Describe the morphology of the erythrocytes.
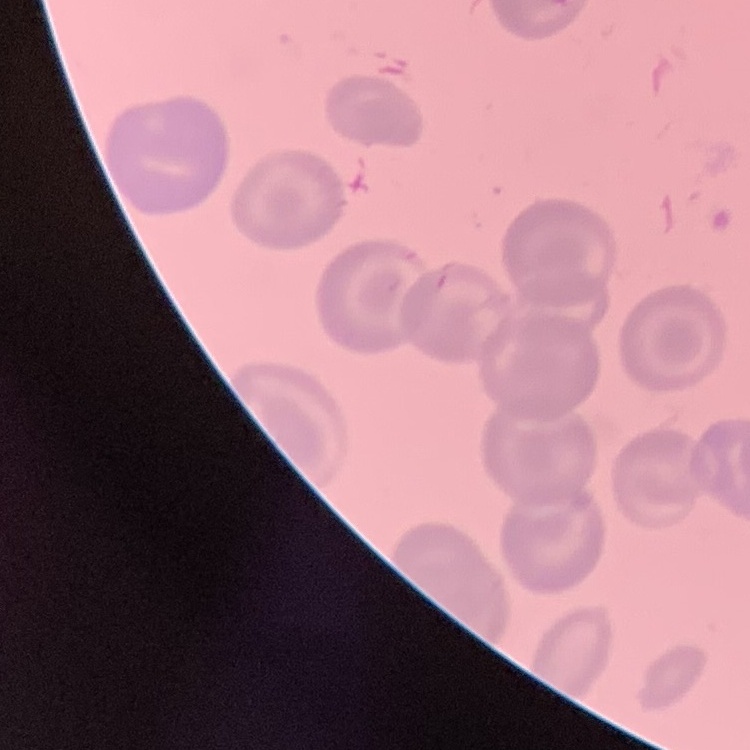
They show no rouleaux formation.

Summary:
  - Stain: Field's or Giemsa
  - Preparation: thin blood smear
  - Image type: square crop of a larger photomicrograph